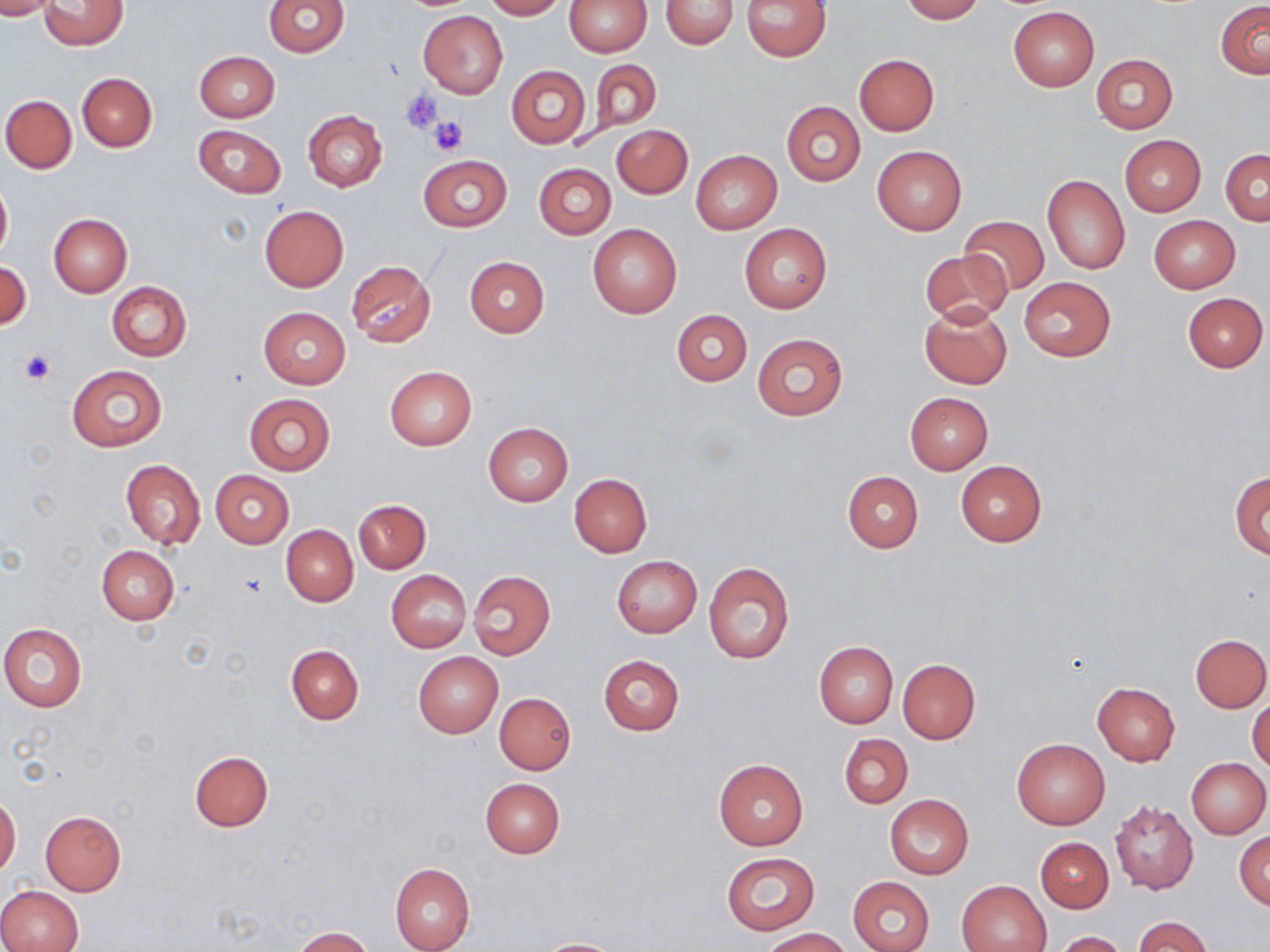 Approximate bounding boxes as (x1,y1)-(x2,y2) corner pairs in pixels. Platelet locations: (400,89)-(445,132), (429,117)-(468,157), (19,350)-(56,385). Uninfected red blood cell locations: (0,0)-(57,19), (39,0)-(127,50), (265,0)-(350,57), (485,0)-(565,19), (563,0)-(652,56), (660,0)-(739,48), (741,0)-(832,62), (899,0)-(984,22), (1215,0)-(1270,79), (1007,7)-(1098,92), (419,10)-(508,98), (194,51)-(279,123), (1090,53)-(1178,133), (855,54)-(939,135), (590,59)-(661,136), (506,65)-(591,149), (77,73)-(157,152), (2,95)-(76,171), (782,102)-(865,186), (303,111)-(387,191), (193,124)-(286,197), (611,124)-(692,198), (1120,135)-(1205,215), (873,146)-(966,233), (1221,148)-(1270,224), (690,149)-(781,235), (417,154)-(511,231), (533,162)-(616,239), (1042,175)-(1130,276), (0,180)-(12,262), (259,205)-(349,292), (49,214)-(132,298), (1149,215)-(1239,292), (960,216)-(1048,294), (588,224)-(681,318), (740,224)-(832,313), (919,247)-(1012,325), (464,256)-(549,337), (1,260)-(31,329), (346,261)-(436,348), (1019,277)-(1115,359), (106,282)-(191,361), (1183,292)-(1268,372), (920,303)-(1012,389), (258,307)-(350,389), (671,309)-(751,386), (752,333)-(847,420), (68,364)-(167,452), (384,366)-(477,451), (905,392)-(992,474), (243,393)-(335,475), (482,423)-(572,506), (120,459)-(206,549), (955,460)-(1046,546), (210,470)-(293,549), (1230,470)-(1269,559), (843,471)-(923,552), (568,472)-(652,557), (354,499)-(430,572), (281,525)-(358,606), (97,545)-(178,624), (610,554)-(702,638), (703,561)-(795,664), (386,569)-(471,653), (467,570)-(556,660), (0,623)-(88,711), (1191,633)-(1270,712), (814,642)-(897,727), (287,645)-(363,725), (413,652)-(503,737), (599,655)-(684,736), (897,659)-(980,742), (1091,682)-(1181,765), (1249,691)-(1270,774), (495,693)-(576,774), (839,734)-(913,808), (1011,738)-(1109,829), (189,750)-(273,832), (1186,757)-(1269,839), (714,758)-(808,850), (479,778)-(565,858), (885,794)-(974,879), (0,795)-(21,877), (1110,799)-(1198,895), (40,811)-(126,895), (1235,830)-(1270,909), (1036,837)-(1113,912), (721,851)-(820,935), (390,862)-(475,952), (848,875)-(935,952), (957,879)-(1050,952), (0,885)-(84,952), (1134,917)-(1214,952), (292,927)-(375,952), (760,928)-(853,951), (1053,931)-(1128,951), (532,938)-(628,952). Slide-level diagnosis: no evidence of blood parasites. Single field of view. May-Grünwald-Giemsa-stained preparation. Thin blood film. Image is 1270×952 pixels. Captured at 1000x magnification. Optical microscopy.